Report the malaria status of this cell.
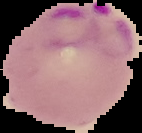

It is parasitized.

image_size: 142×133 pixels
preparation: thin blood smear
image_type: segmented cell region with the area outside set to black